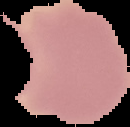

Segmented cell region on a black background. Image is 130×127 pixels. Malaria status: uninfected. From a thin blood smear.